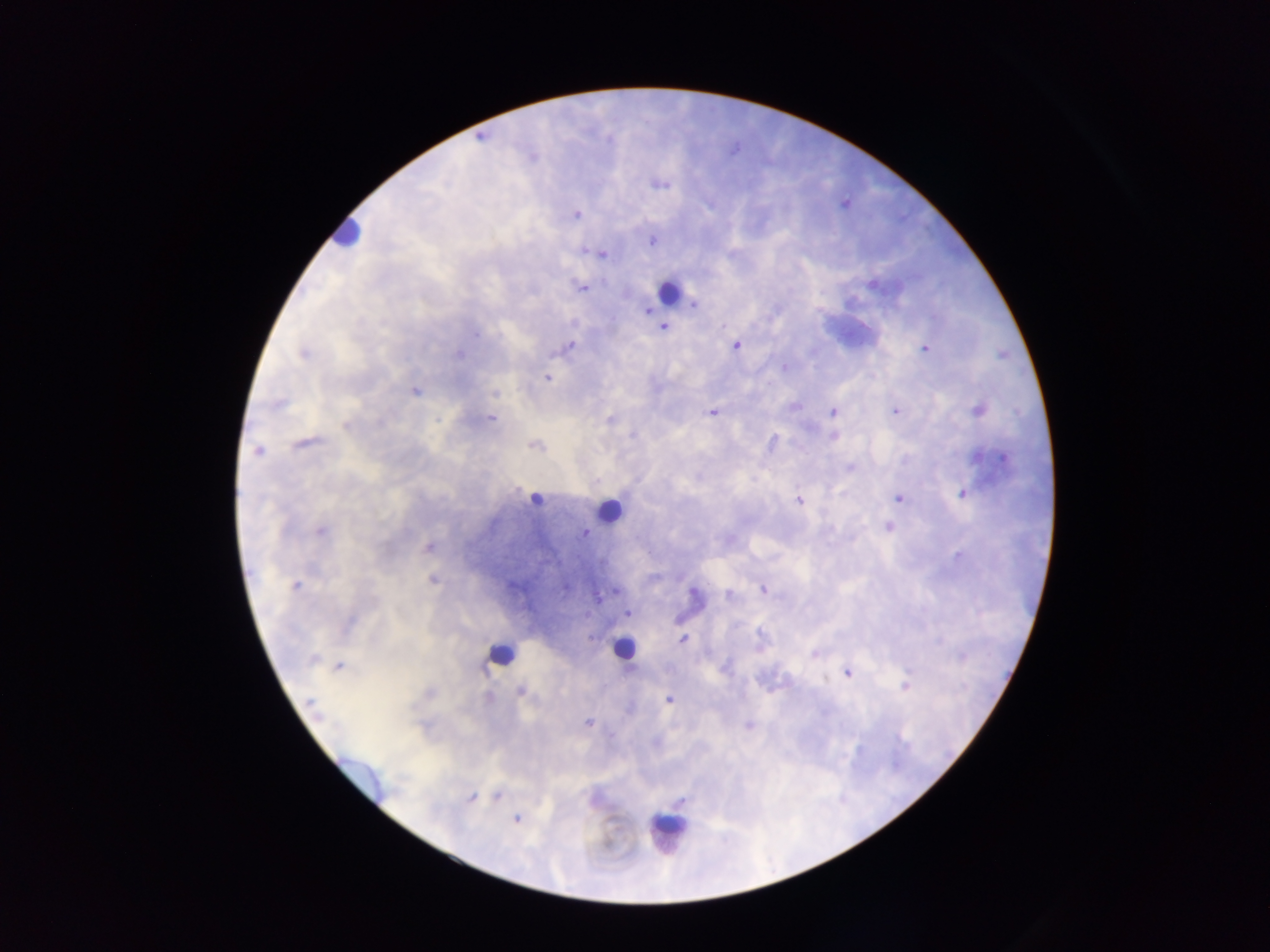

Approximate centers as (x, y) in pixels.
Summary:
  - Leukocyte locations (subset; some below the resolvable size): (344, 234), (667, 297), (536, 499), (608, 509), (623, 648), (499, 655), (670, 830)
  - Plasmodium parasite locations: (658, 183), (576, 215), (652, 241), (585, 252), (599, 254), (872, 284), (582, 287), (694, 304), (647, 310), (663, 327), (477, 334), (570, 346), (736, 346), (925, 349), (303, 354), (459, 354), (784, 367), (547, 378), (415, 391), (494, 394), (277, 404), (794, 406), (833, 411), (894, 411), (979, 411), (712, 413), (491, 418), (610, 420), (345, 426), (631, 434), (834, 436), (772, 442), (303, 444), (534, 445), (258, 450), (976, 456), (1005, 458), (849, 467), (963, 493), (899, 498), (798, 500), (888, 527), (319, 530), (585, 533), (429, 547), (957, 556), (432, 579), (295, 586), (763, 589), (616, 590), (729, 594), (627, 613), (682, 639), (815, 653), (313, 659), (339, 666), (847, 672), (905, 686), (520, 691), (668, 699), (310, 702), (589, 723), (748, 725), (497, 796), (471, 797), (680, 801), (516, 819)
  - Capture: mobile-phone photograph through a microscope
  - Image size: 1270×952 pixels
  - Field of view: single
  - Country: Ghana
  - Preparation: thick blood smear